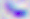

Summary:
  - Magnification: 400x
  - Modality: micrograph
  - Identification: Toxoplasma gondii